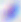

magnification = 400x
modality = photomicrograph
identification = Toxoplasma gondii